Assess the morphology of the erythrocytes.
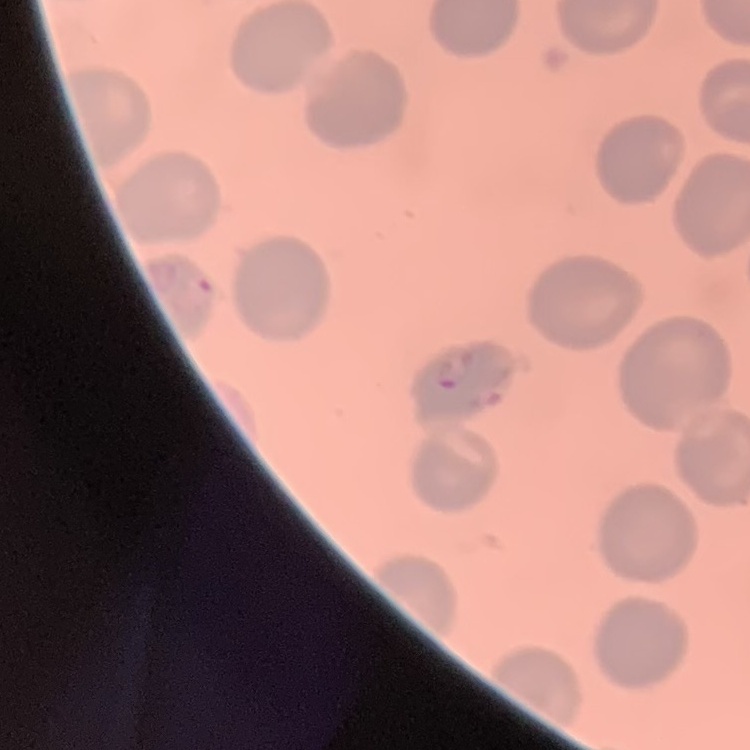
No rouleaux formation.

stain = Field's or Giemsa
preparation = thin peripheral smear
image type = square crop of a larger photomicrograph